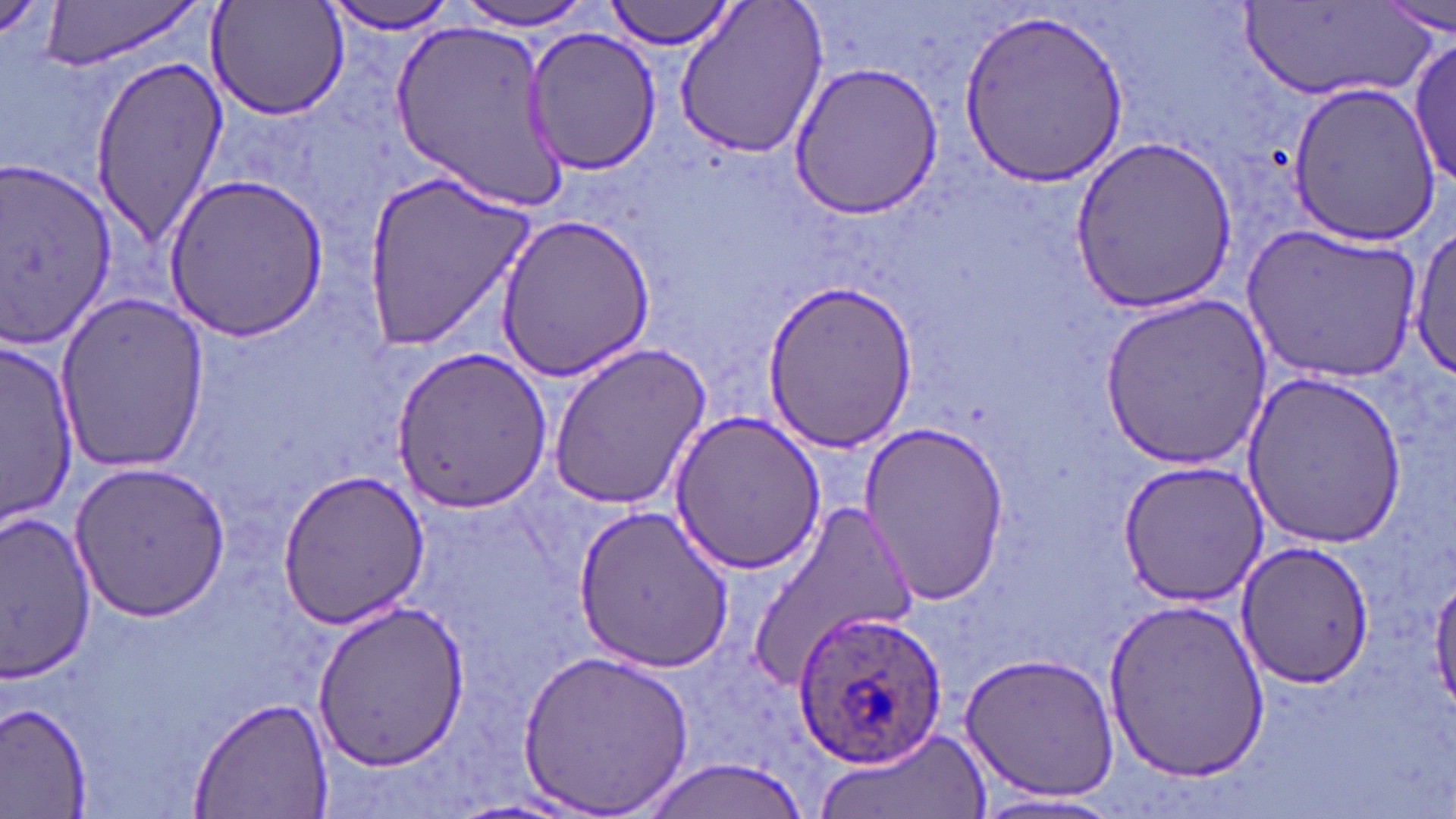

Summary:
  - Coordinate format: approximate bounding boxes as (x1,y1)-(x2,y2) corner pairs in pixels
  - Plasmodium ovale-infected red blood cell locations: (792,608)-(950,770)
  - Uninfected red blood cell locations: (38,0)-(203,73), (607,0)-(736,51), (673,0)-(830,160), (319,1)-(459,36), (208,2)-(348,122), (453,2)-(600,32), (1378,4)-(1454,39), (1241,7)-(1429,105), (956,8)-(1132,188), (387,17)-(569,213), (521,26)-(663,177), (1411,34)-(1456,191), (86,55)-(225,248), (790,61)-(948,221), (1286,81)-(1444,245), (1066,137)-(1245,311), (0,160)-(118,355), (362,172)-(535,350), (160,174)-(334,342), (492,213)-(661,382), (1242,223)-(1422,384), (1410,228)-(1456,382), (762,277)-(918,453), (55,291)-(211,473), (1100,293)-(1271,468), (2,340)-(80,528), (546,344)-(713,512), (389,346)-(552,516), (1240,372)-(1409,549), (667,410)-(826,575), (859,419)-(1013,604), (69,460)-(230,623), (1118,461)-(1267,606), (276,469)-(430,629), (745,500)-(921,685), (572,504)-(733,673), (2,511)-(100,684), (1233,538)-(1379,686), (1430,576)-(1456,709), (1100,600)-(1275,782), (311,602)-(473,771), (516,647)-(697,815), (959,651)-(1121,802), (188,696)-(334,819), (0,703)-(92,816), (814,721)-(992,819), (632,758)-(823,819), (969,792)-(1130,817)
  - Slide-level diagnosis: Plasmodium ovale
  - Modality: light microscopy
  - Magnification: 1000x
  - Preparation: thin blood film
  - Field of view: single
  - Stain: May-Grünwald-Giemsa
  - Image size: 1456×819 pixels